Classify this cell by malaria status.
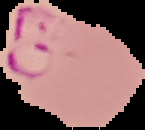
It is parasitized.

image size = 145×130 pixels
preparation = thin blood smear
image type = cell region segmented out of the field of view; surrounding area masked to black